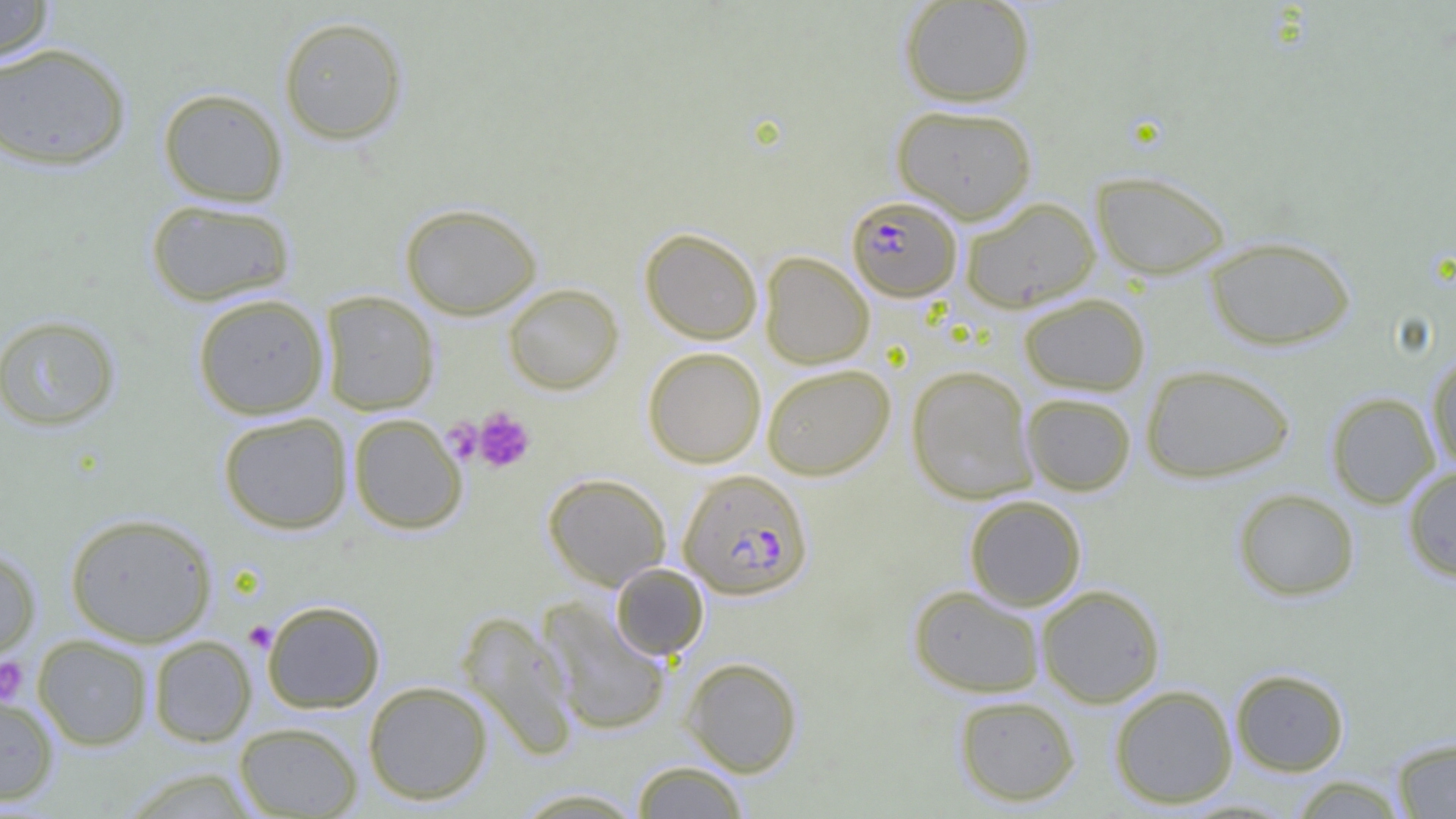
Summary:
  - Coordinate format: approximate bounding boxes as (x1,y1)-(x2,y2) corner pairs in pixels
  - Plasmodium falciparum-infected red blood cell locations: (847,195)-(962,301), (678,469)-(813,599)
  - Uninfected red blood cell locations: (0,0)-(57,62), (898,1)-(1036,107), (278,15)-(408,145), (0,42)-(132,171), (158,88)-(288,207), (892,104)-(1038,223), (1091,170)-(1232,279), (959,196)-(1101,312), (145,198)-(297,307), (400,202)-(542,319), (640,228)-(763,345), (1204,235)-(1356,350), (759,251)-(875,369), (502,283)-(624,395), (319,291)-(440,415), (1018,292)-(1151,396), (192,293)-(330,419), (0,314)-(121,432), (642,347)-(767,468), (1427,350)-(1456,473), (761,363)-(895,480), (1140,363)-(1296,483), (906,365)-(1038,504), (1021,392)-(1136,496), (1326,392)-(1441,508), (217,412)-(353,534), (348,413)-(468,534), (1402,466)-(1456,582), (543,473)-(671,590), (1232,488)-(1360,601), (964,495)-(1087,611), (64,512)-(217,647), (0,547)-(40,662), (610,564)-(709,660), (1036,584)-(1165,707), (908,585)-(1046,698), (538,598)-(673,736), (261,599)-(386,713), (457,610)-(579,760), (33,635)-(153,750), (148,635)-(256,746), (680,657)-(804,776), (1230,668)-(1350,776), (363,680)-(493,805), (1109,685)-(1238,809), (0,689)-(60,807), (953,694)-(1081,807), (234,721)-(363,818), (1391,736)-(1456,818), (631,761)-(749,818), (118,767)-(264,818), (1289,776)-(1409,818), (509,787)-(649,818)
  - Platelet locations: (472,407)-(536,474), (441,417)-(482,464), (244,621)-(277,653), (0,657)-(31,705)
  - Slide-level diagnosis: Plasmodium falciparum
  - Image size: 1456×819 pixels
  - Magnification: 1000x
  - Modality: optical microscopy
  - Field of view: one of a larger specimen
  - Preparation: thin blood smear